Assess the morphology of the red blood cells.
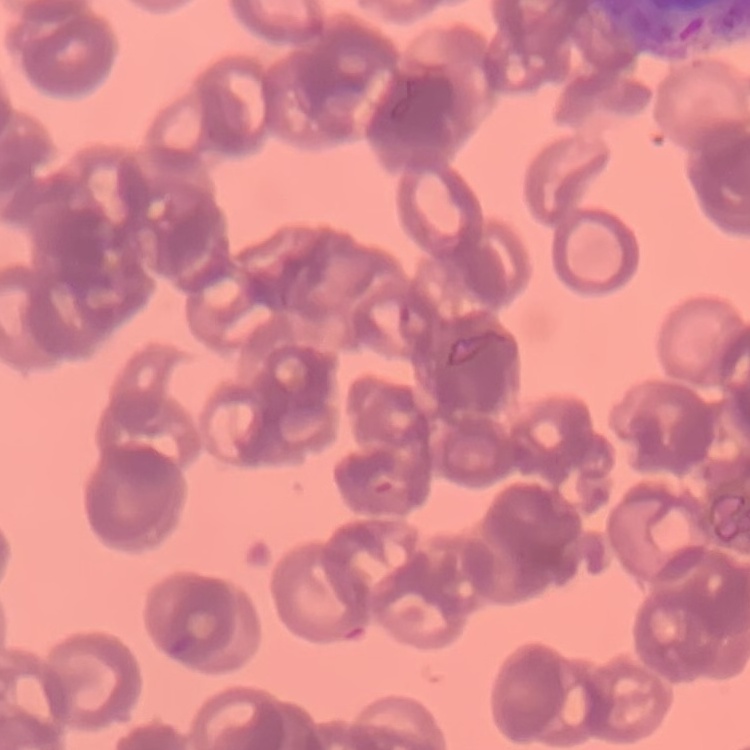

Rouleaux formation.

{
  "stain": "Field's or Giemsa",
  "image_type": "one tile cut from a larger photomicrograph",
  "preparation": "thin blood smear"
}